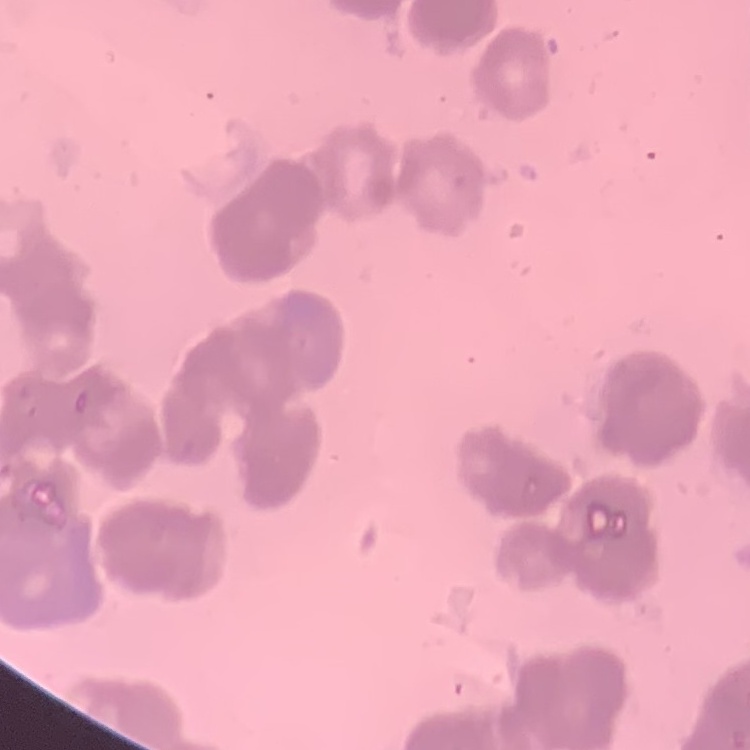

Summary:
  - Erythrocyte morphology: rouleaux formation
  - Image type: square crop of a larger photomicrograph
  - Stain: Field's or Giemsa
  - Preparation: thin blood film